Evaluate for malaria.
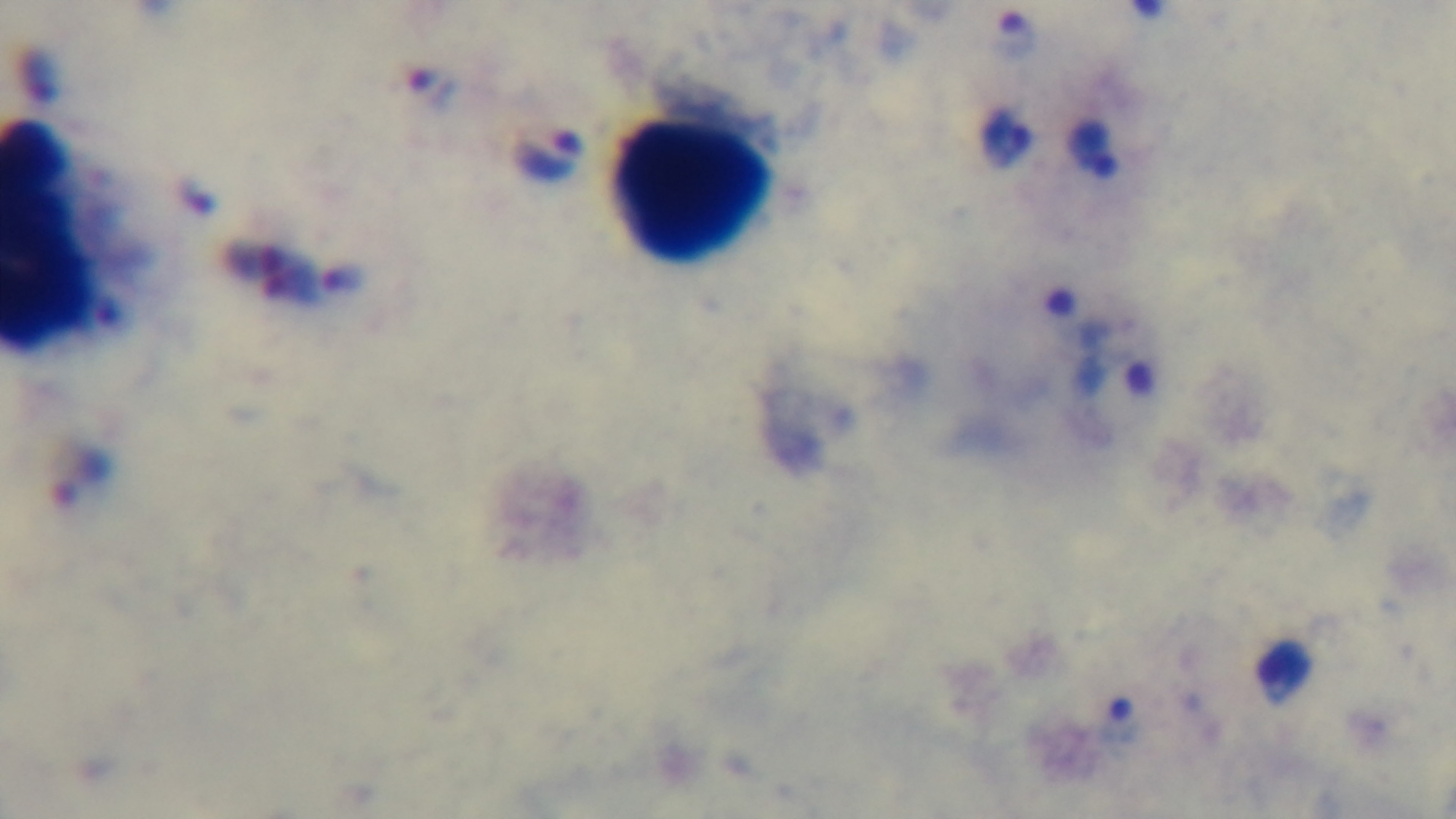
It is infected.

Summary:
  - Capture: mounted 4K digital camera
  - Objective: 100x oil immersion
  - Modality: light microscopy
  - Field of view: single
  - Stain: Giemsa
  - Preparation: thick blood film